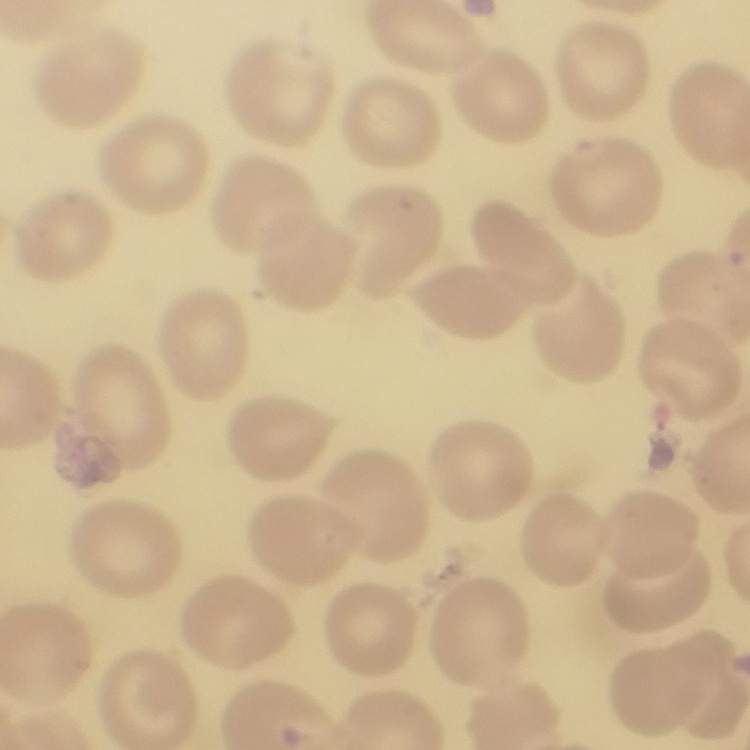
erythrocyte morphology = no rouleaux formation
stain = Field's or Giemsa
preparation = thin peripheral smear
image type = one tile cut from a larger photomicrograph